Assess this cell for malaria.
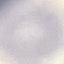

It is uninfected.

{
  "preparation": "thin blood film",
  "stain": "Giemsa",
  "image_type": "cell patch, automatically extracted from a larger field of view and resized to 64 × 64 pixels",
  "capture": "smartphone camera at the microscope eyepiece"
}